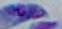

Summary:
  - Modality: micrograph
  - Magnification: 1000x
  - Identification: Toxoplasma gondii